Name the parasite shown.
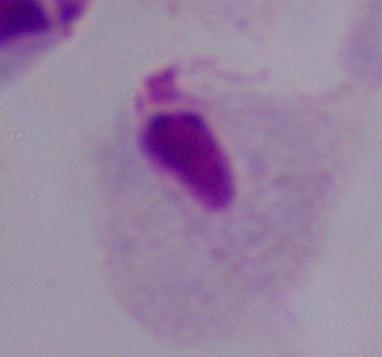
A trichomonad.

Summary:
  - Magnification: 1000x
  - Modality: micrograph